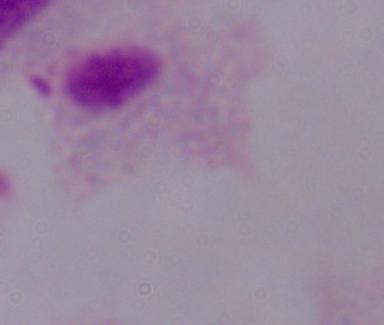

identification = trichomonad
modality = photomicrograph
magnification = 1000x